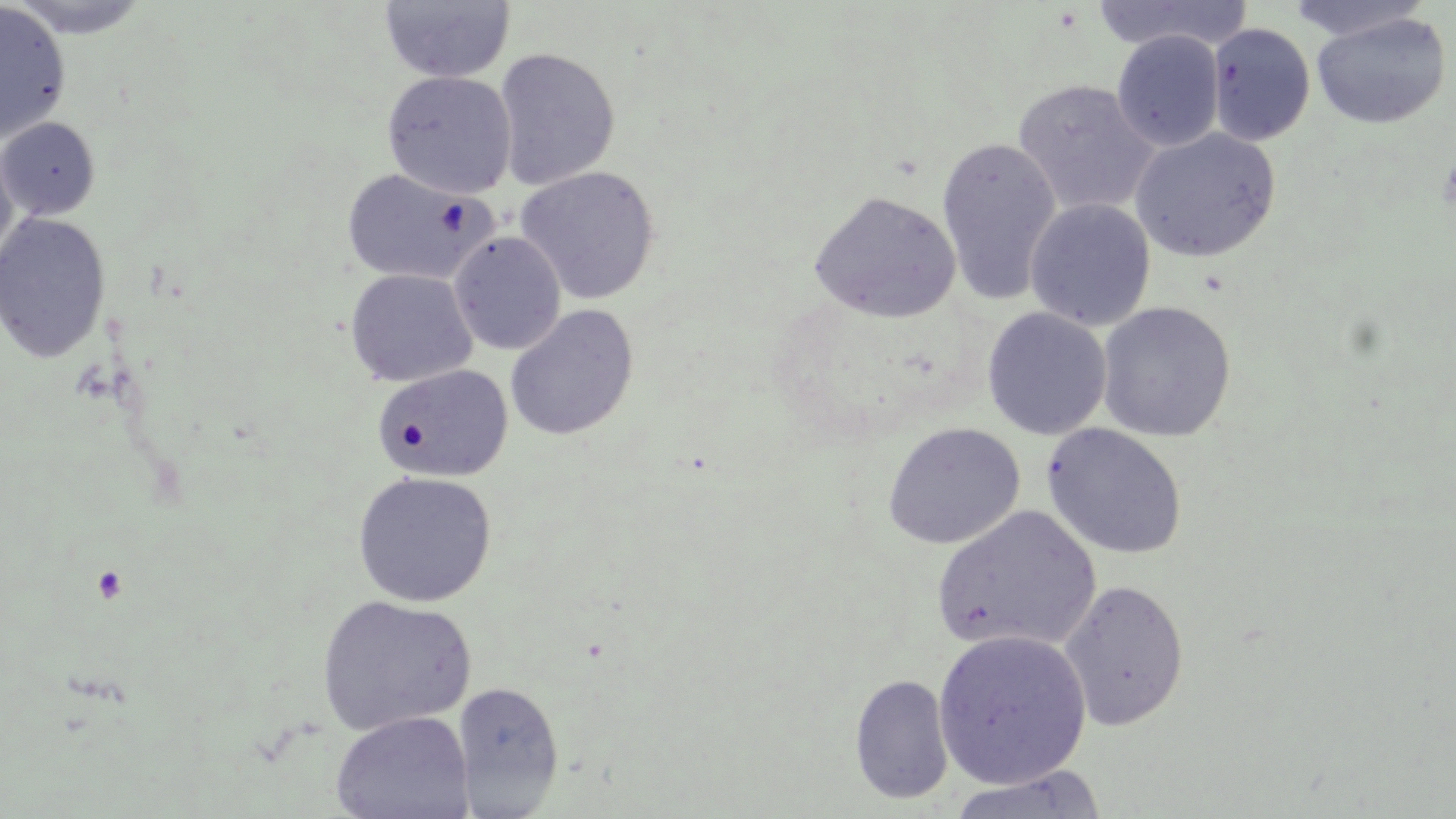

slide-level diagnosis = negative for blood parasites
modality = light microscopy
field of view = one of a larger specimen
image size = 1456×819 pixels
uninfected red blood cell locations = approximate bounding boxes as [x1, y1, x2, y2] in pixels: [3, 0, 156, 39], [379, 0, 516, 83], [1091, 0, 1252, 54], [1286, 0, 1434, 42], [0, 1, 72, 144], [1311, 11, 1451, 128], [1207, 24, 1315, 145], [1111, 30, 1224, 152], [493, 47, 621, 191], [382, 70, 517, 199], [1012, 80, 1160, 217], [1, 117, 100, 221], [1129, 128, 1281, 263], [935, 137, 1061, 307], [0, 138, 19, 267], [515, 165, 661, 305], [341, 167, 498, 285], [809, 191, 961, 323], [1025, 199, 1156, 331], [1, 211, 111, 364], [449, 232, 566, 355], [344, 268, 477, 388], [1096, 300, 1236, 441], [505, 304, 639, 442], [982, 307, 1111, 440], [373, 364, 513, 483], [881, 421, 1025, 550], [1042, 423, 1188, 560], [352, 471, 497, 607], [931, 505, 1100, 653], [1058, 578, 1190, 731], [316, 595, 476, 736], [932, 629, 1092, 789], [849, 673, 954, 805], [452, 680, 565, 817], [330, 710, 475, 819], [944, 766, 1108, 819]
magnification = 1000x
preparation = thin blood smear
stain = May-Grünwald-Giemsa